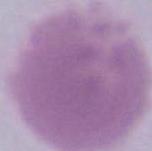

identification = red blood cell
magnification = 1000x
modality = photomicrograph